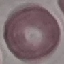
Summary:
  - Malaria status: uninfected
  - Stain: Giemsa
  - Preparation: thin blood film
  - Capture: smartphone through the microscope eyepiece
  - Image type: automatically extracted cell patch, resized to 64 × 64 pixels